Name the parasite shown.
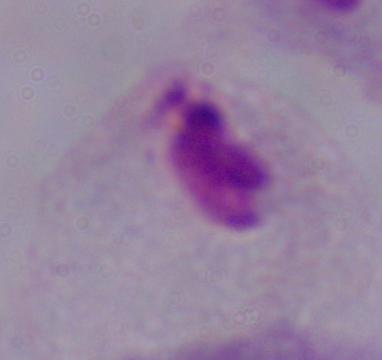
This is a trichomonad.

modality = photomicrograph
magnification = 1000x